Point out each Plasmodium parasite.
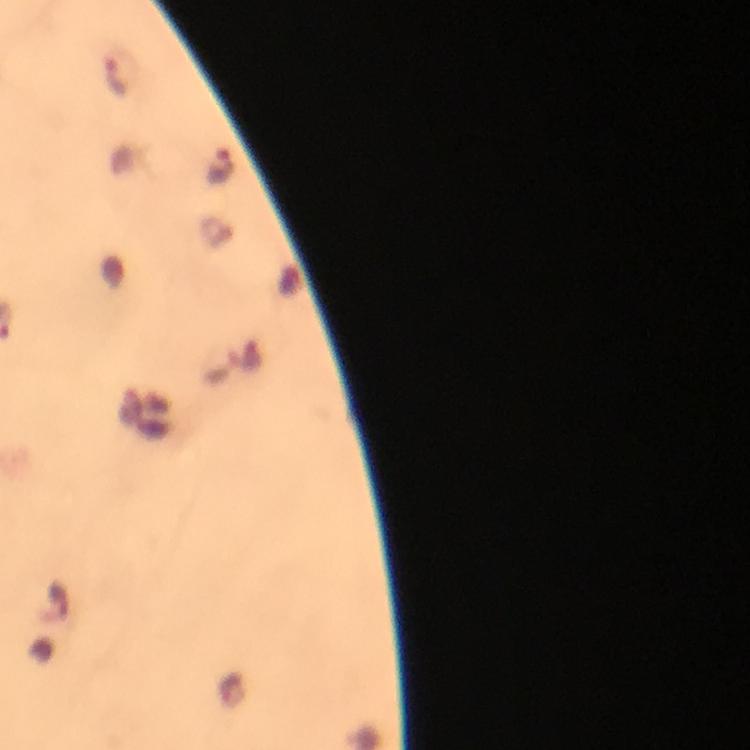
Approximate centers as {x, y} in pixels.
Plasmodium parasites: {118, 74}, {222, 167}.

Image is 750×750 pixels. Photographed with a smartphone mounted on the microscope. Giemsa-stained preparation. A crop from one field of view. Thick blood film. Immersion oil was used. At 100x magnification. From a diagnostic examination for malaria.